Classify this cell by malaria status.
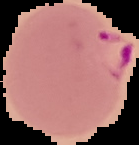
It is parasitized.

From a thin blood film. Image is 139×145 pixels. Segmented cell region on a black background.